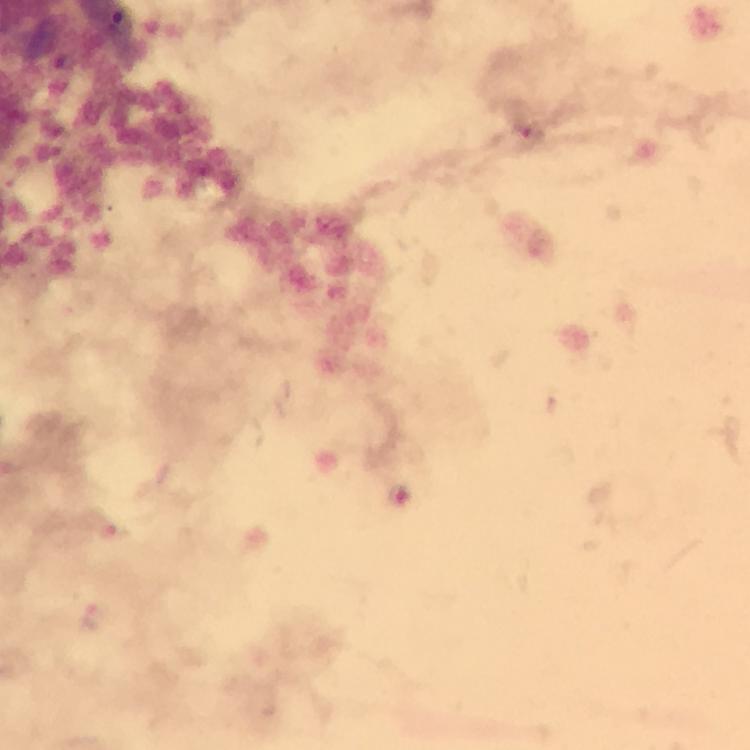
Approximate centers as [x, y] in pixels.
Summary:
  - Malaria parasite locations: [531, 135], [404, 495], [110, 533], [91, 617]
  - Magnification: 100x
  - Cropped from: a single field of view
  - Preparation: thick smear
  - Capture: smartphone camera through the microscope
  - Immersion oil: used
  - Stain: Giemsa
  - Image size: 750×750 pixels
  - Context: from a malaria diagnostic workup